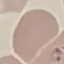

Result: no malaria parasites seen. Giemsa stain. Thin smear of blood. Photographed with a smartphone camera at the microscope eyepiece. Automatically extracted cell patch, resized to 64 × 64 pixels.